Point out leukocytes.
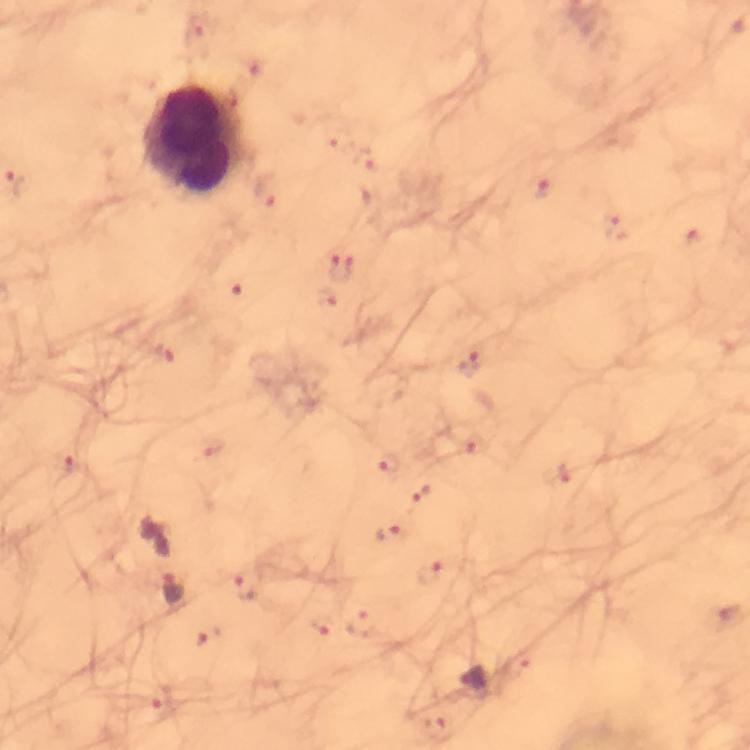
Approximate centers as {x, y} in pixels.
Leukocytes: {190, 139}.

Summary:
  - Malaria parasite locations: {196, 31}, {339, 138}, {367, 160}, {544, 190}, {623, 225}, {693, 239}, {343, 267}, {240, 289}, {331, 302}, {165, 353}, {471, 363}, {475, 446}, {70, 464}, {387, 464}, {561, 473}, {421, 494}, {387, 534}, {430, 572}, {247, 589}, {173, 590}, {360, 623}, {317, 629}, {519, 663}, {161, 701}, {434, 726}
  - Preparation: thick blood smear
  - Stain: Giemsa
  - Image size: 750×750 pixels
  - Capture: smartphone mounted on the microscope
  - Immersion oil: used
  - Magnification: 100x
  - Context: from a diagnostic examination for malaria
  - Cropped from: one field of view